State which parasite is depicted.
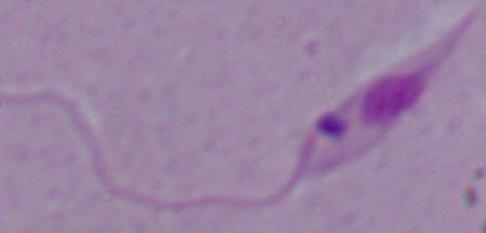

Leishmania.

Micrograph. Captured at 1000x magnification.